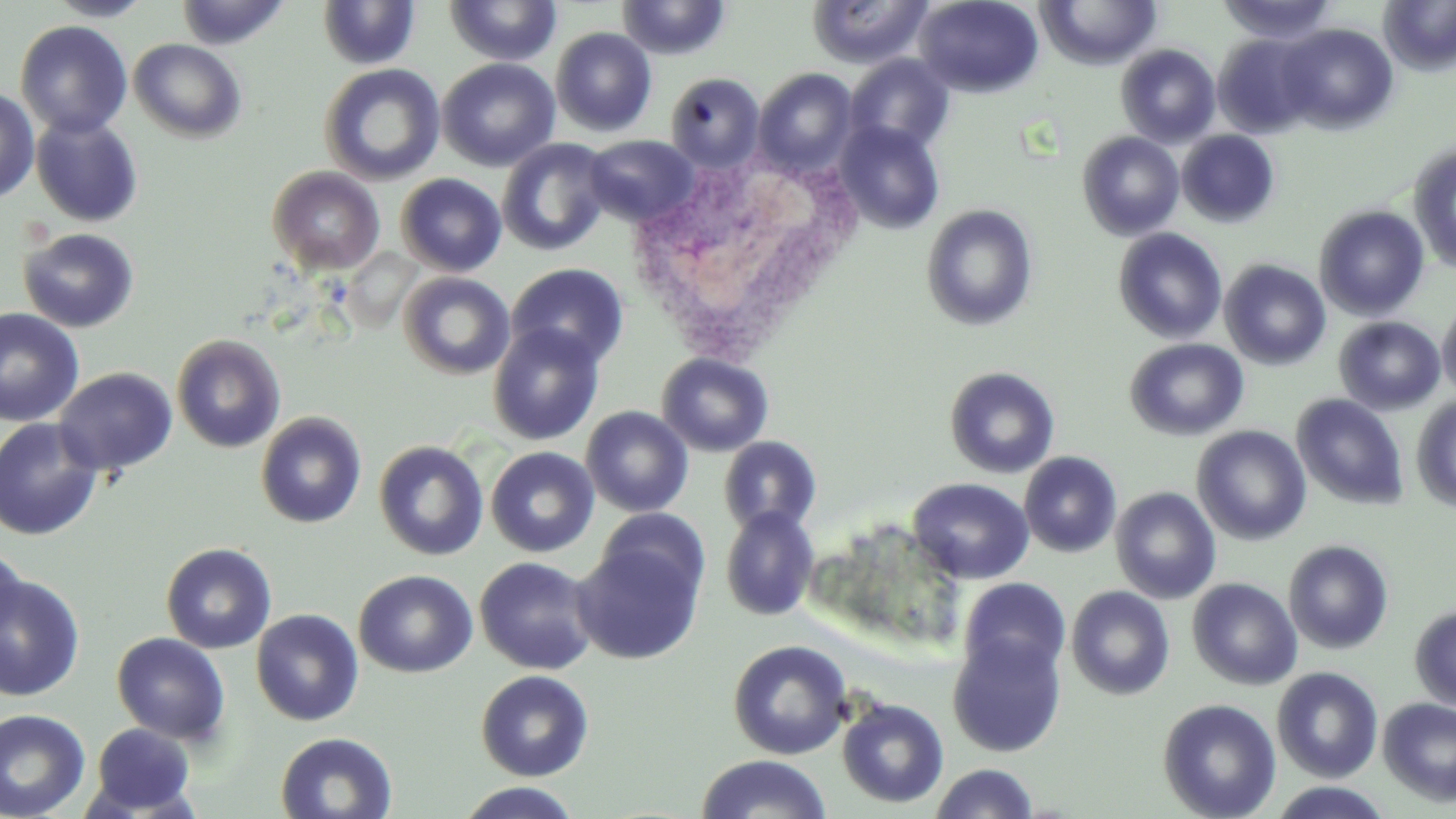

Approximate bounding boxes as (x1,y1)-(x2,y2) corner pairs in pixels. White blood cell locations: (627,152)-(857,368). Uninfected red blood cell locations: (46,0)-(154,21), (176,0)-(291,50), (616,0)-(732,60), (806,0)-(933,69), (913,0)-(1045,98), (1038,0)-(1161,70), (1218,0)-(1339,44), (1380,0)-(1456,75), (317,1)-(420,69), (444,1)-(562,67), (15,20)-(133,138), (1277,23)-(1398,134), (551,27)-(657,137), (1213,34)-(1319,139), (129,38)-(247,143), (1116,44)-(1221,147), (844,54)-(955,155), (437,58)-(560,171), (319,63)-(445,185), (753,68)-(858,176), (665,72)-(765,172), (0,85)-(40,202), (30,114)-(144,227), (834,120)-(945,235), (1176,130)-(1280,227), (1077,132)-(1184,240), (584,135)-(697,226), (497,137)-(612,256), (1408,142)-(1456,275), (267,166)-(385,275), (396,173)-(507,276), (921,205)-(1038,331), (1314,205)-(1429,320), (18,227)-(140,332), (1113,228)-(1227,344), (1219,259)-(1331,370), (507,263)-(629,369), (399,272)-(514,379), (1437,296)-(1456,403), (0,308)-(84,427), (1333,316)-(1446,415), (487,323)-(606,446), (171,334)-(286,453), (1124,338)-(1248,440), (656,352)-(774,457), (944,365)-(1060,479), (54,367)-(177,477), (1292,393)-(1409,510), (1411,395)-(1456,512), (581,405)-(693,517), (255,411)-(367,528), (0,417)-(103,540), (1192,425)-(1311,545), (719,435)-(822,535), (374,440)-(489,561), (486,446)-(599,558), (1018,451)-(1122,558), (908,477)-(1034,584), (1111,486)-(1221,604), (720,506)-(820,621), (596,508)-(709,605), (1283,539)-(1394,654), (572,540)-(704,665), (160,542)-(277,654), (0,548)-(26,642), (474,556)-(600,675), (354,570)-(477,678), (0,573)-(85,701), (959,577)-(1071,682), (1187,578)-(1302,690), (1066,585)-(1175,700), (1409,604)-(1456,709), (251,609)-(364,726), (112,632)-(230,744), (948,633)-(1067,757), (728,640)-(852,760), (1272,667)-(1383,782), (476,670)-(594,781), (837,697)-(949,808), (1157,698)-(1281,819), (1377,698)-(1456,806), (0,709)-(91,819), (90,722)-(196,814), (274,731)-(398,817), (696,754)-(832,818), (929,763)-(1040,819), (456,782)-(584,818), (1265,782)-(1396,818). Slide-level diagnosis: no evidence of blood parasites. Single field of view. Captured at 1000x magnification. Thin blood smear. Light microscopy. May-Grünwald-Giemsa-stained preparation. Image is 1456×819 pixels.